Locate every blood parasite and identify its species.
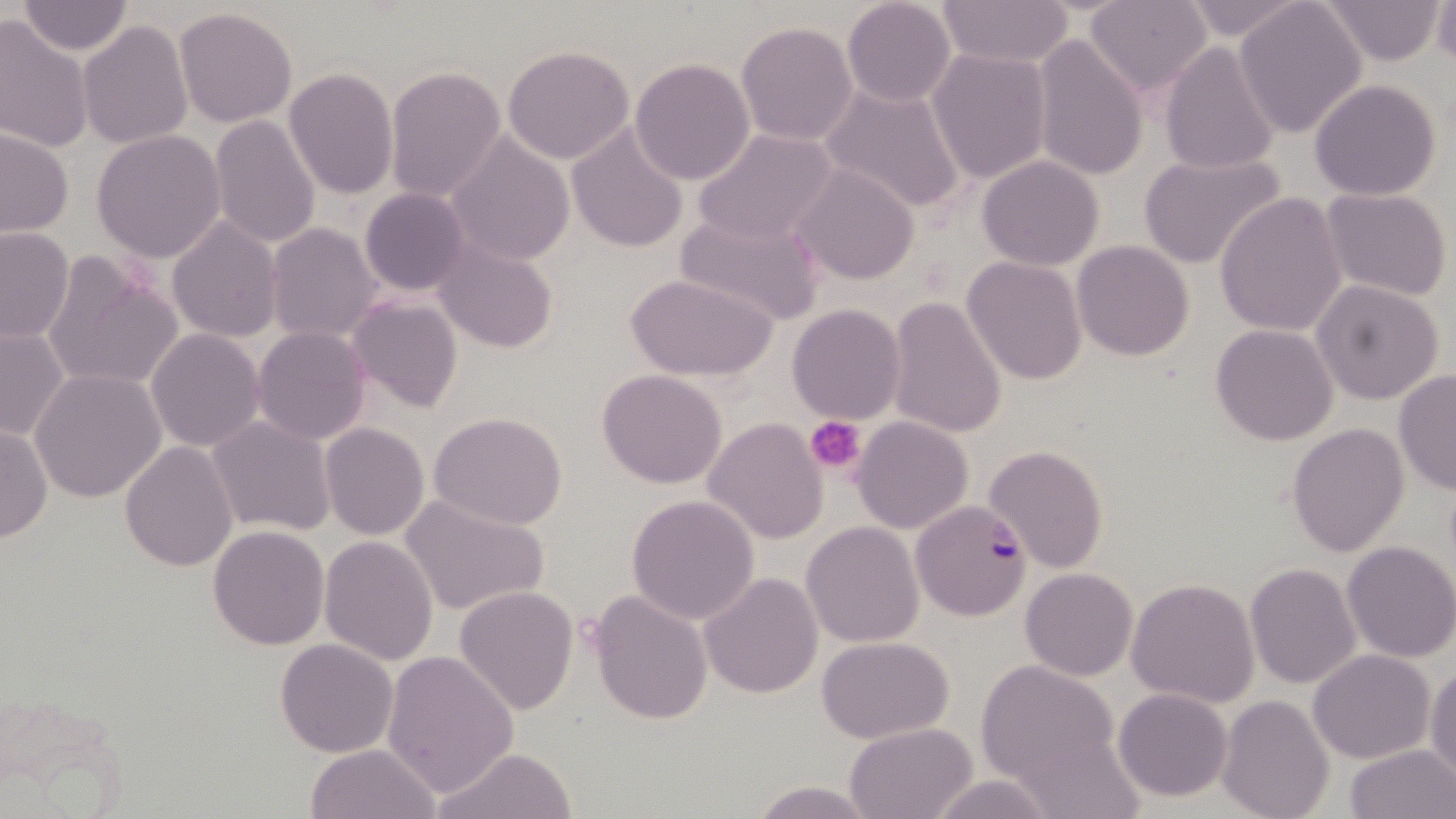
Approximate bounding boxes as (x1,y1)-(x2,y2) corner pairs in pixels.
Plasmodium falciparum-infected red blood cells: (910,501)-(1031,621).
No Plasmodium ovale, Plasmodium malariae, Plasmodium vivax, Babesia divergens, or Trypanosoma brucei observed.

Summary:
  - Uninfected red blood cell locations: (841,0)-(957,108), (936,0)-(1073,70), (1083,0)-(1212,98), (1177,0)-(1312,42), (1234,0)-(1369,138), (1319,0)-(1445,65), (1431,0)-(1455,69), (17,2)-(134,55), (174,7)-(299,129), (0,17)-(93,153), (78,19)-(193,151), (735,21)-(859,147), (1031,35)-(1147,182), (1158,40)-(1279,175), (501,44)-(635,165), (926,47)-(1053,183), (629,58)-(757,186), (384,64)-(508,204), (282,68)-(398,198), (1309,79)-(1443,201), (818,81)-(967,216), (208,115)-(322,248), (566,124)-(689,251), (0,126)-(73,237), (693,127)-(840,248), (91,129)-(225,264), (445,132)-(577,266), (1136,150)-(1287,269), (977,156)-(1104,271), (792,165)-(920,286), (1319,187)-(1453,302), (359,189)-(471,296), (1215,191)-(1349,337), (674,209)-(825,326), (166,218)-(282,341), (266,223)-(382,346), (0,227)-(74,343), (433,240)-(558,354), (1072,240)-(1194,362), (42,251)-(185,395), (962,258)-(1086,386), (627,273)-(776,383), (1311,280)-(1445,404), (887,295)-(1009,439), (348,296)-(463,412), (788,304)-(904,423), (1210,324)-(1338,446), (0,326)-(70,442), (252,327)-(373,445), (147,329)-(265,450), (1393,367)-(1456,496), (30,368)-(168,503), (596,369)-(728,491), (428,413)-(569,530), (207,415)-(334,536), (851,416)-(975,535), (704,418)-(827,542), (1287,422)-(1409,558), (1,423)-(51,545), (320,423)-(430,540), (119,440)-(237,573), (984,444)-(1108,572), (399,493)-(548,616), (627,494)-(760,625), (802,521)-(925,647), (206,525)-(329,649), (319,535)-(438,666), (1340,540)-(1456,663), (1245,562)-(1362,689), (1021,567)-(1137,680), (698,571)-(822,699), (1125,576)-(1260,708), (453,586)-(578,715), (587,590)-(713,726), (817,637)-(952,743), (275,638)-(399,757), (1307,648)-(1435,764), (382,651)-(517,798), (975,660)-(1124,795), (1427,663)-(1456,786), (1113,687)-(1233,802), (1216,694)-(1335,819), (844,723)-(976,819), (1009,727)-(1147,818), (1343,743)-(1455,819), (303,744)-(441,819), (428,746)-(579,819), (923,774)-(1064,818), (746,779)-(882,819)
  - Platelet locations: (808,418)-(864,474)
  - Slide-level diagnosis: Plasmodium falciparum
  - Stain: May-Grünwald-Giemsa
  - Preparation: thin blood film
  - Field of view: single
  - Image size: 1456×819 pixels
  - Magnification: 1000x
  - Modality: light microscopy